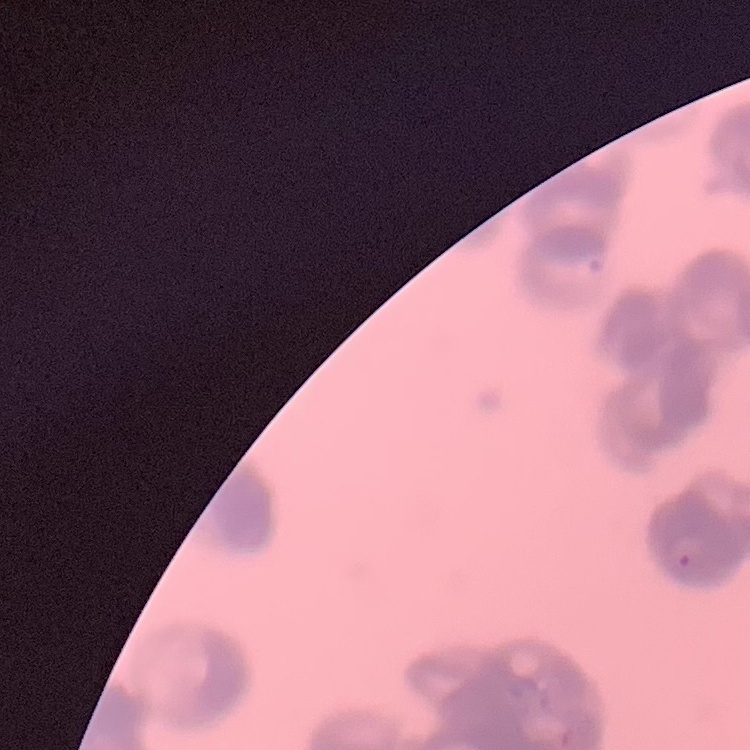

erythrocyte morphology = rouleaux formation
image type = one tile cut from a larger photomicrograph
preparation = thin blood smear
stain = Field's or Giemsa